Point out each Plasmodium parasite.
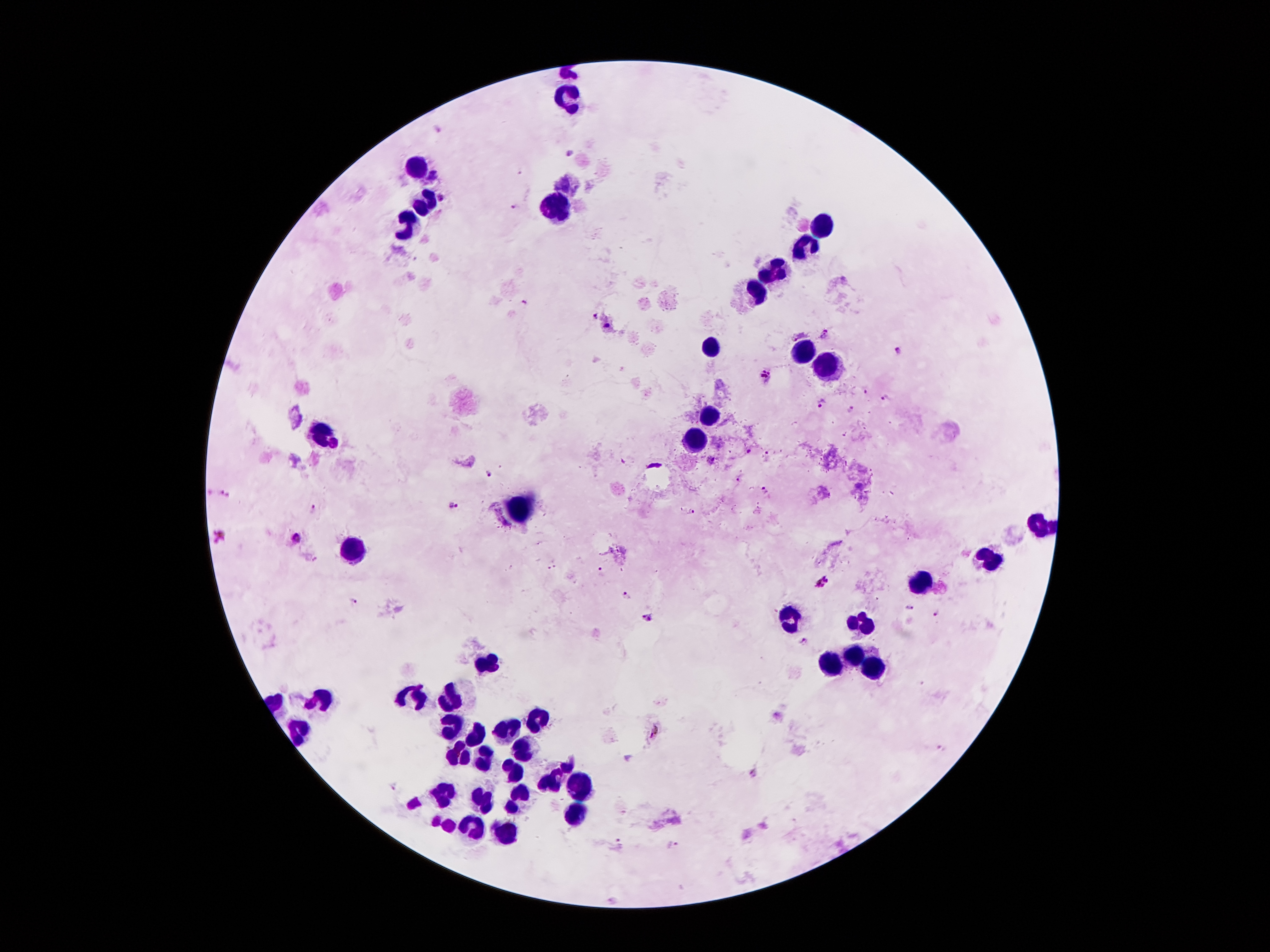

Approximate object centers, in pixels from the top-left corner.
Plasmodium parasites: (x=568, y=153), (x=433, y=176), (x=513, y=204), (x=524, y=302), (x=595, y=315), (x=608, y=325), (x=825, y=333), (x=797, y=336), (x=900, y=352), (x=765, y=374), (x=865, y=389), (x=886, y=398), (x=821, y=403), (x=850, y=409), (x=334, y=444), (x=748, y=452), (x=767, y=453), (x=490, y=477), (x=738, y=480), (x=765, y=490), (x=225, y=494), (x=452, y=505), (x=314, y=508), (x=692, y=512), (x=220, y=535), (x=296, y=538), (x=599, y=572), (x=823, y=581), (x=625, y=592), (x=354, y=601), (x=935, y=613), (x=648, y=617), (x=656, y=731), (x=753, y=773), (x=393, y=787), (x=619, y=842), (x=673, y=845).

magnification: 100x
preparation: thick blood film
patient_malaria_status: infected with Plasmodium falciparum
capture: smartphone camera through the microscope eyepiece
field_of_view: single
stain: Giemsa
image_size: 1270×952 pixels
leukocyte_locations: 'approximate object centers, in pixels from the top-left corner: (x=570, y=99), (x=414, y=166), (x=427, y=202), (x=553, y=212), (x=408, y=225), (x=822, y=227), (x=805, y=248), (x=776, y=271), (x=759, y=292), (x=715, y=348), (x=801, y=348), (x=822, y=365), (x=708, y=418), (x=314, y=432), (x=696, y=441), (x=519, y=510), (x=1042, y=521), (x=354, y=552), (x=988, y=560), (x=923, y=584), (x=788, y=621), (x=860, y=626), (x=851, y=655), (x=486, y=663), (x=830, y=663), (x=872, y=665), (x=412, y=695), (x=320, y=699), (x=448, y=701), (x=538, y=720), (x=452, y=726), (x=297, y=730), (x=509, y=730), (x=473, y=735), (x=456, y=754), (x=521, y=754), (x=482, y=762), (x=509, y=772), (x=555, y=779), (x=574, y=787), (x=442, y=793), (x=479, y=798), (x=517, y=798), (x=570, y=817), (x=471, y=829), (x=507, y=833)'